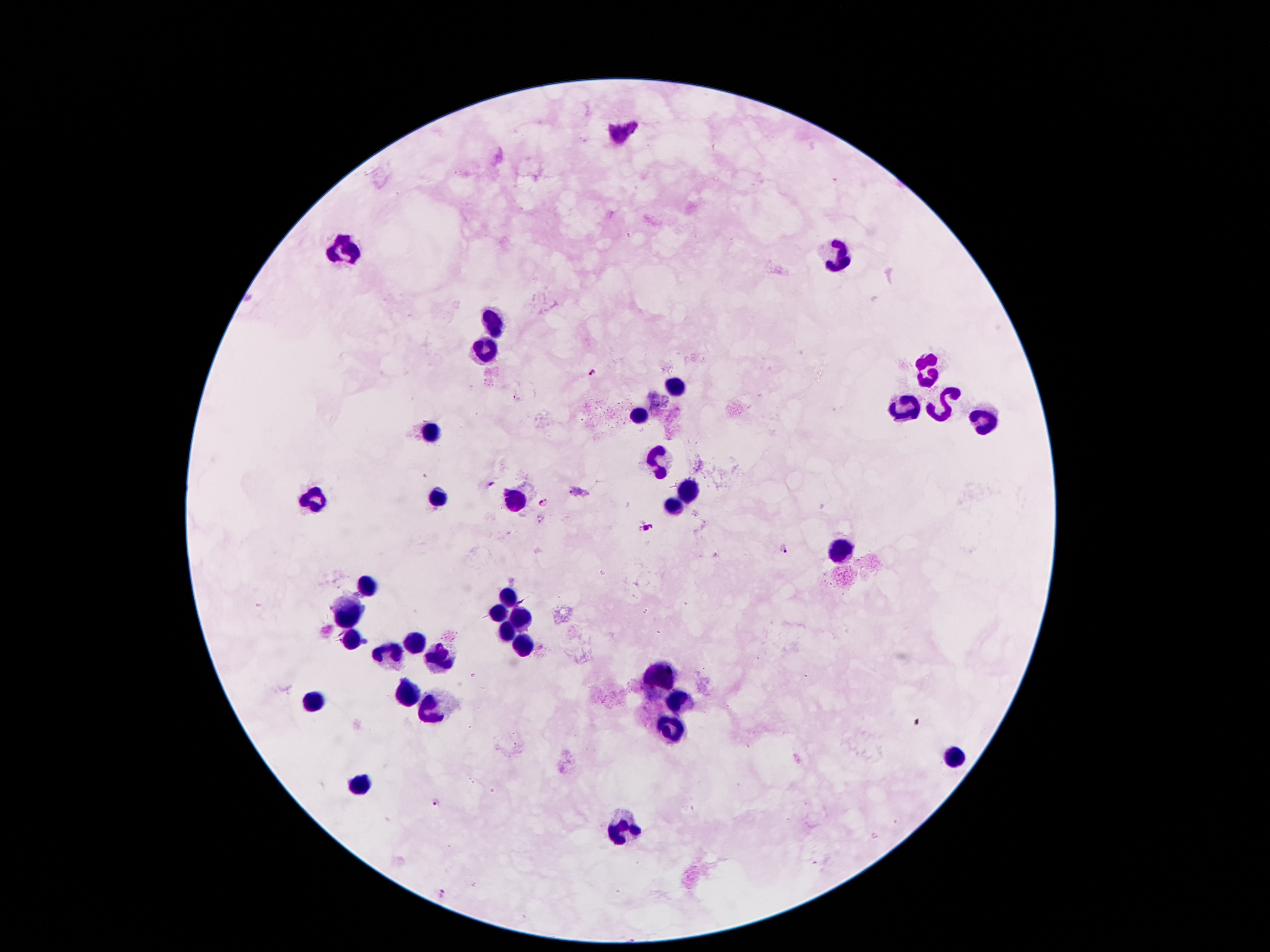

Approximate object centers, in pixels from the top-left corner.
Summary:
  - Leukocyte locations: (x=621, y=132), (x=346, y=246), (x=841, y=258), (x=494, y=323), (x=485, y=345), (x=923, y=374), (x=677, y=386), (x=945, y=401), (x=905, y=407), (x=641, y=415), (x=984, y=419), (x=430, y=433), (x=659, y=462), (x=687, y=486), (x=437, y=496), (x=314, y=497), (x=518, y=500), (x=673, y=508), (x=841, y=551), (x=369, y=585), (x=507, y=600), (x=351, y=609), (x=498, y=612), (x=521, y=612), (x=509, y=630), (x=350, y=639), (x=410, y=641), (x=523, y=643), (x=385, y=653), (x=441, y=657), (x=661, y=676), (x=407, y=691), (x=314, y=703), (x=682, y=705), (x=430, y=710), (x=671, y=727), (x=950, y=757), (x=357, y=787), (x=621, y=830)
  - Plasmodium parasite locations: (x=592, y=373), (x=490, y=486), (x=543, y=502), (x=645, y=525), (x=784, y=550), (x=437, y=803), (x=442, y=896)
  - Capture: smartphone camera through the microscope eyepiece
  - Field of view: one from this slide
  - Stain: Giemsa
  - Patient malaria status: infected with Plasmodium falciparum
  - Magnification: 100x
  - Image size: 1270×952 pixels
  - Preparation: thick peripheral-blood smear